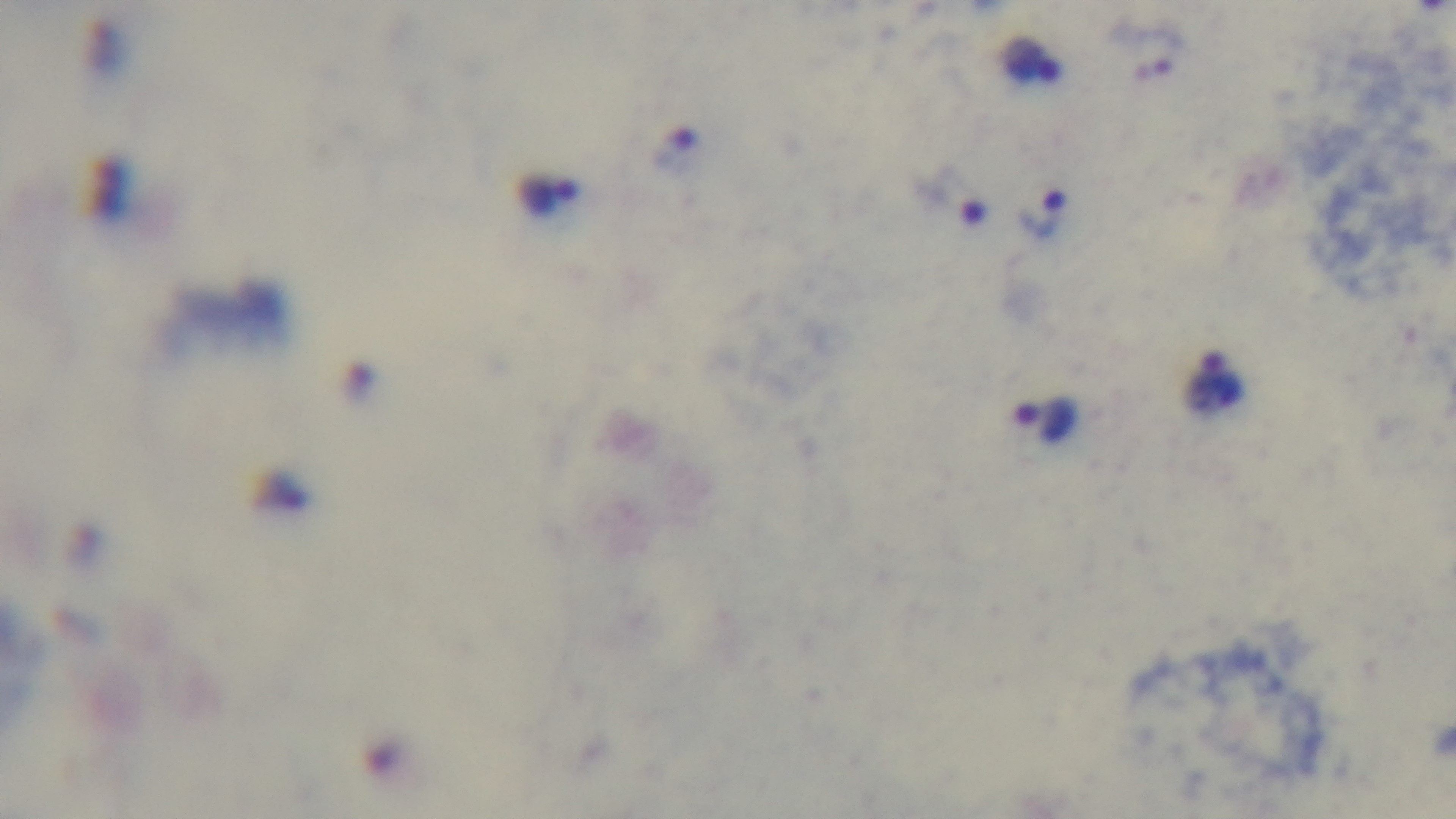 Photomicrograph. Single field of view. Preparation: thick blood film. Oil-immersion objective, 100x. Giemsa stain. Captured with a mounted 4K digital camera. Malaria status: positive.